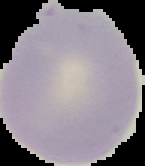
image_type: segmented cell region on a black background
image_size: 145×166 pixels
preparation: thin blood smear
result: no malaria parasites detected